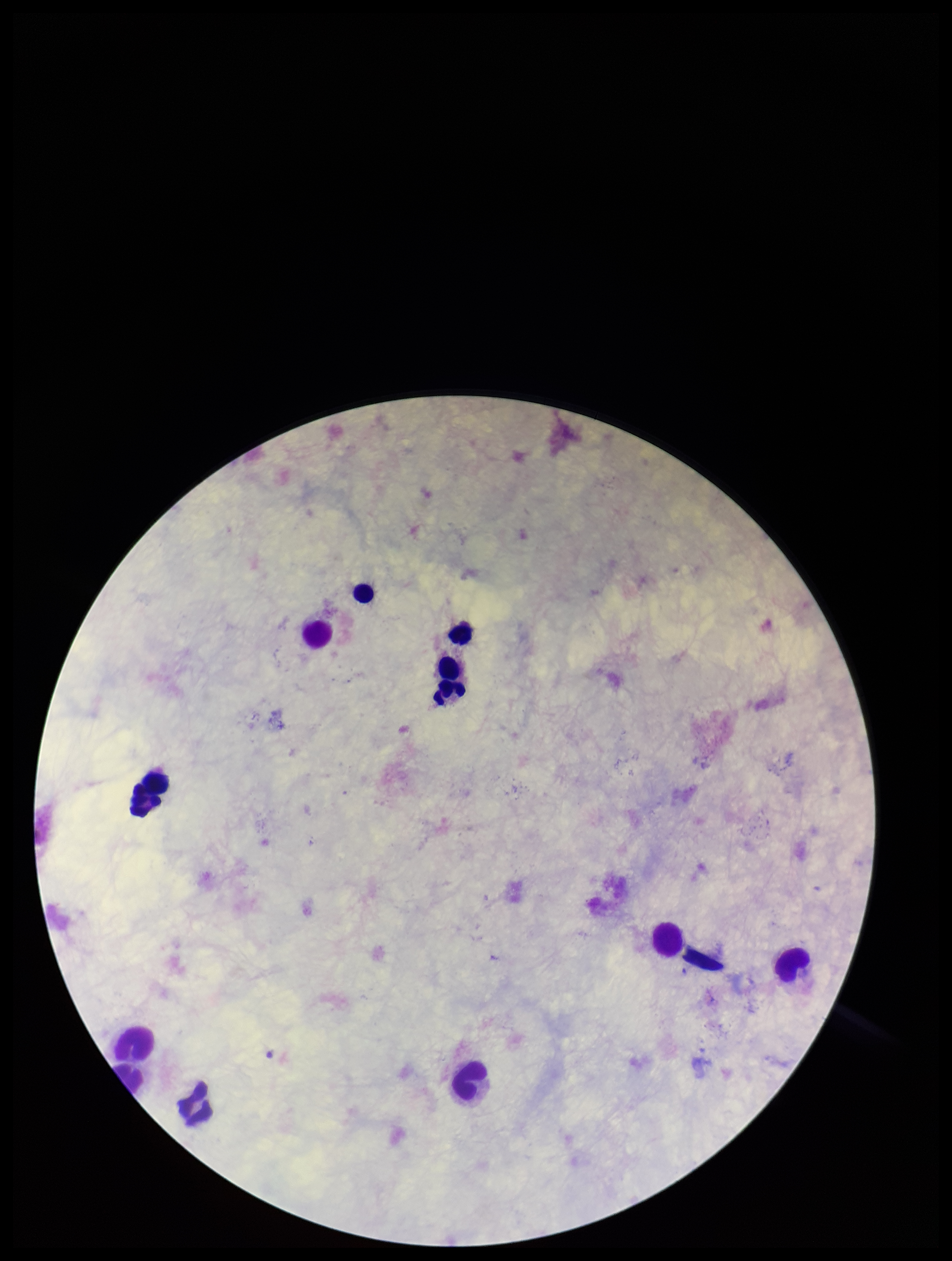
Plasmodium parasites: none seen. Parasite count: 0. Photographed through the microscope eyepiece with a smartphone camera. Preparation: thick blood smear. Image is 952×1261 pixels. One field from this slide. Stained with Giemsa. Patient malaria status: negative. Leukocyte count: 12.